Point out each Plasmodium parasite.
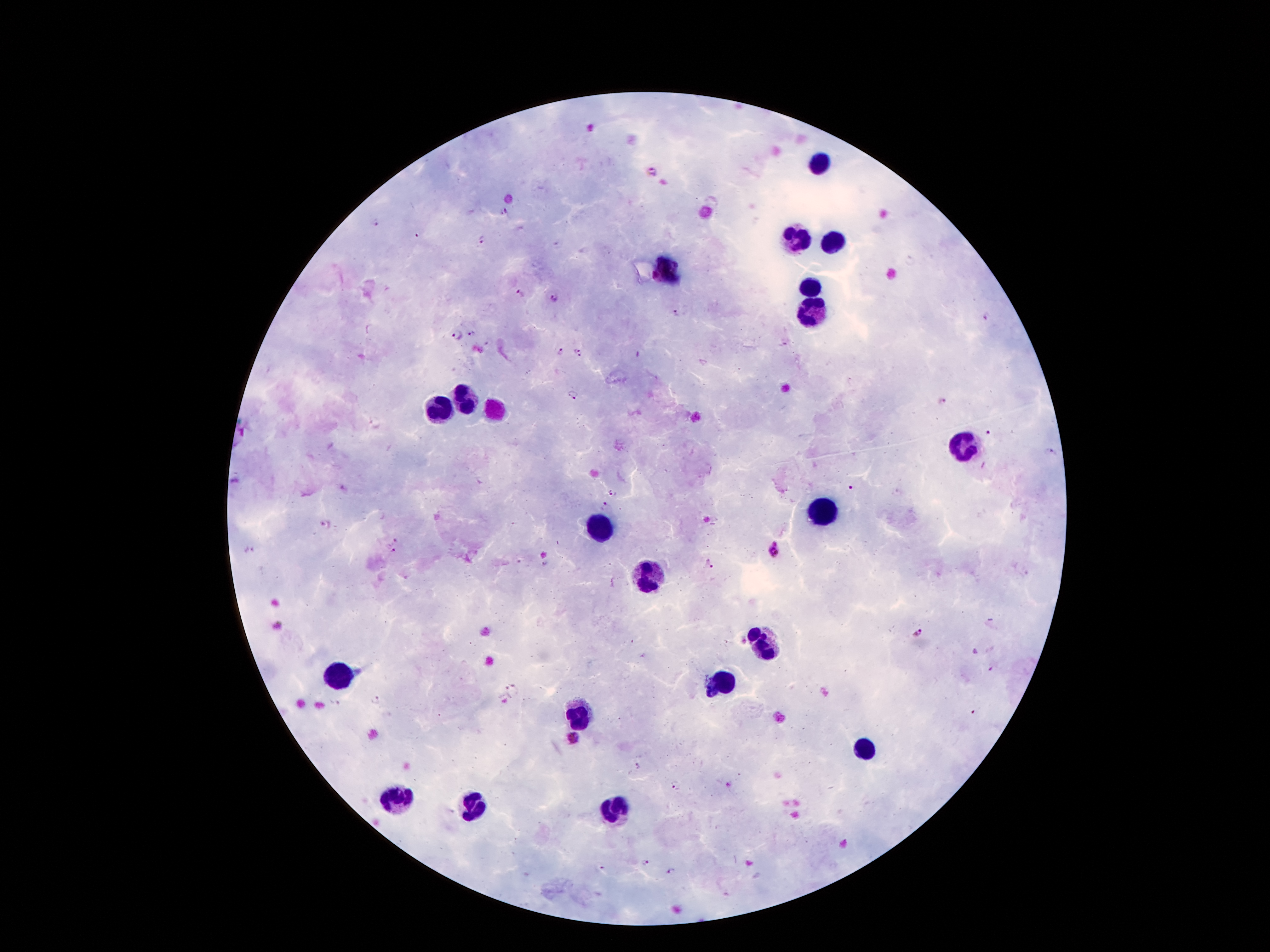

Approximate centers as (x, y) in pixels.
Plasmodium parasites: (651, 171), (504, 209), (378, 221), (481, 240), (559, 246), (908, 260), (654, 275), (521, 294), (554, 298), (678, 314), (986, 316), (471, 333), (457, 334), (488, 343), (560, 352), (578, 354), (638, 355), (571, 395), (943, 401), (988, 433), (1049, 452), (850, 487), (612, 495), (602, 507), (327, 526), (394, 540), (774, 548), (249, 550), (390, 551), (546, 564), (709, 565), (918, 633), (993, 667), (513, 688), (507, 700), (377, 701), (334, 703), (973, 712), (572, 738), (637, 766), (728, 785), (675, 786), (644, 862), (599, 866), (670, 870).

Summary:
  - Leukocyte locations: (819, 164), (796, 239), (832, 244), (664, 268), (808, 290), (813, 312), (463, 401), (438, 409), (962, 444), (826, 508), (602, 526), (648, 575), (761, 644), (338, 676), (718, 685), (582, 717), (864, 751), (399, 799), (473, 801), (614, 805)
  - Stain: Giemsa
  - Preparation: thick blood film
  - Field of view: one from this slide
  - Capture: smartphone through the microscope eyepiece
  - Magnification: 100x
  - Image size: 1270×952 pixels
  - Patient malaria status: infected with Plasmodium falciparum